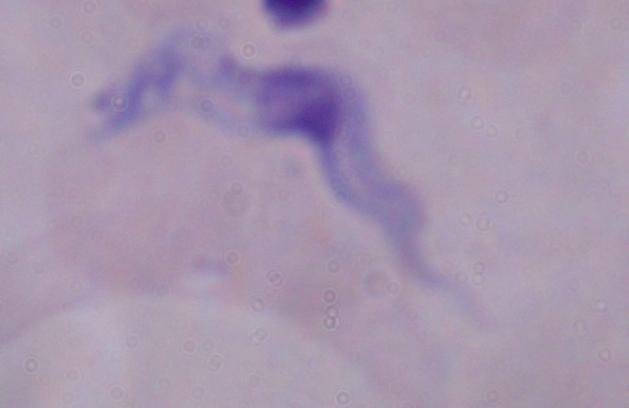

modality = photomicrograph
identification = trypanosome
magnification = 1000x